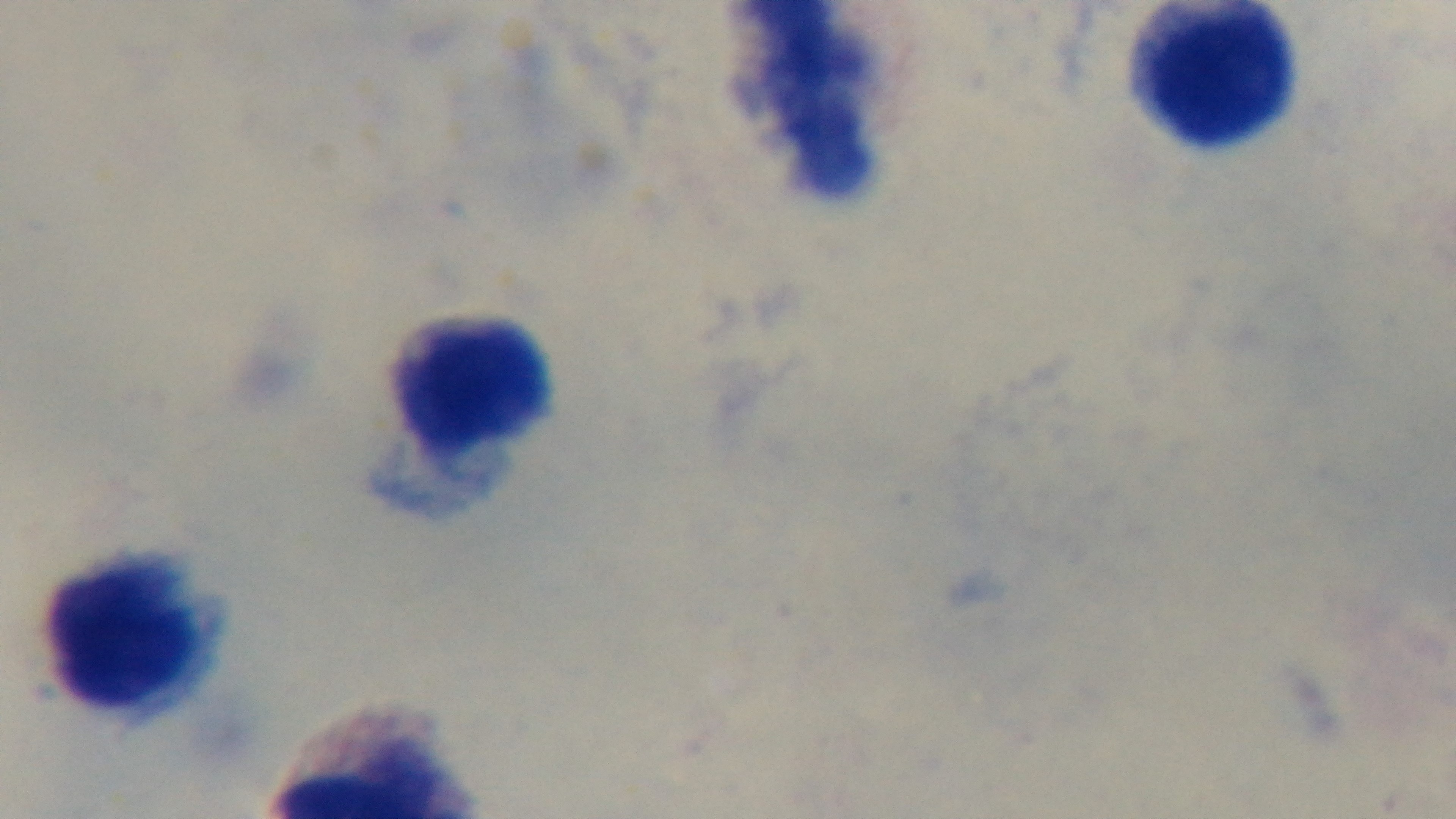

Summary:
  - Preparation: thick blood film
  - Field of view: one from the slide
  - Modality: light microscopy
  - Malaria status: negative
  - Capture: mounted 4K digital camera
  - Objective: 100x oil immersion
  - Stain: Giemsa